Locate and identify every blood parasite.
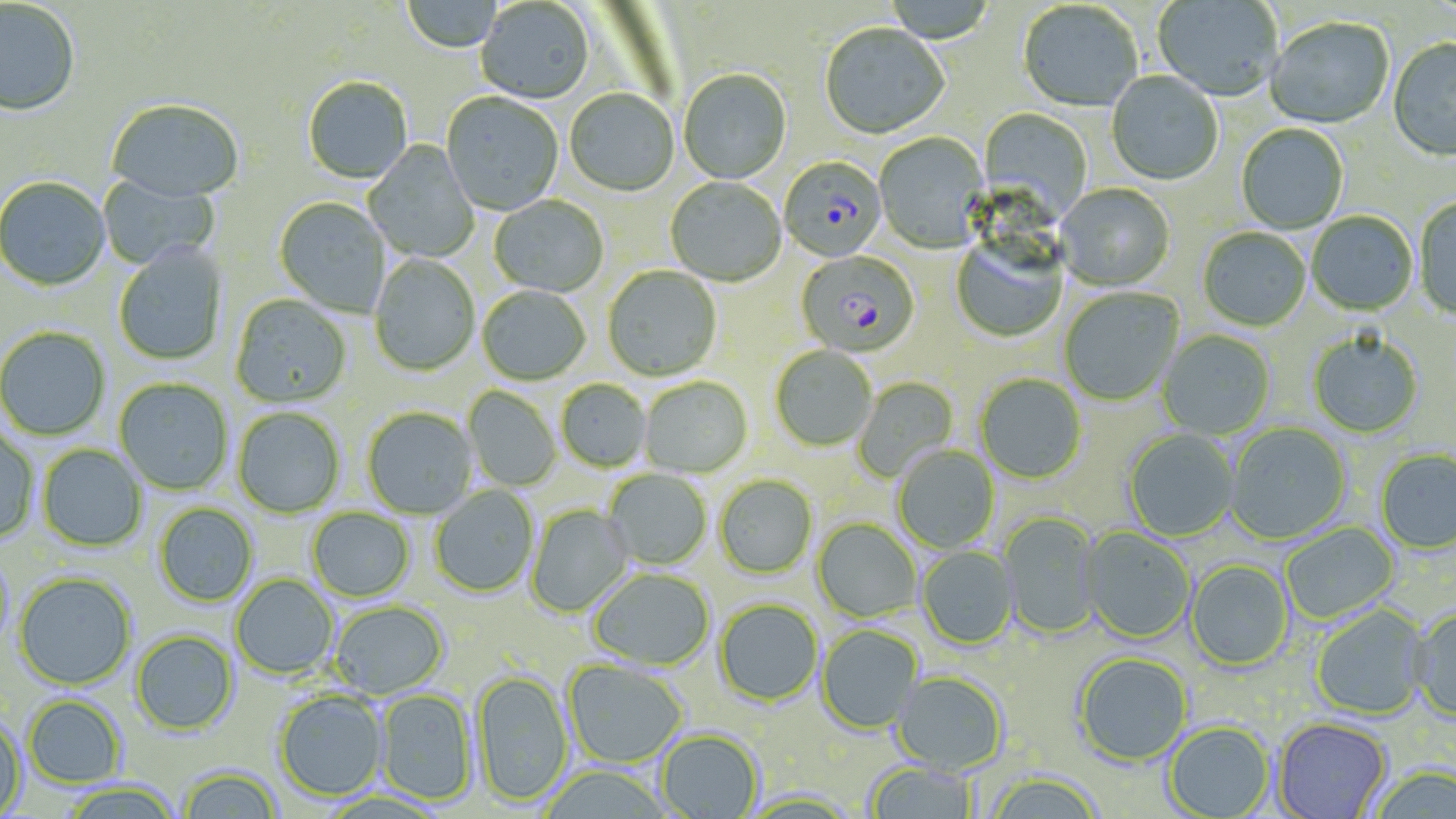
Approximate bounding boxes as (x1, y1, x2, y2) in pixels.
Plasmodium falciparum-infected red blood cells: (779, 158, 886, 263), (796, 251, 919, 358).
No Plasmodium ovale, Plasmodium malariae, Plasmodium vivax, Babesia divergens, or Trypanosoma brucei observed.

Uninfected red blood cell locations: (400, 0, 504, 54), (1153, 0, 1282, 103), (0, 1, 81, 118), (476, 1, 594, 106), (880, 1, 998, 45), (1018, 2, 1142, 113), (1265, 18, 1394, 131), (820, 25, 950, 141), (1388, 39, 1456, 163), (678, 71, 791, 186), (1106, 72, 1223, 187), (303, 78, 413, 186), (565, 91, 679, 198), (441, 94, 563, 217), (106, 101, 245, 206), (978, 108, 1092, 226), (1236, 124, 1349, 235), (874, 133, 989, 254), (363, 141, 480, 263), (97, 173, 219, 271), (0, 178, 110, 292), (665, 178, 786, 288), (1054, 184, 1175, 293), (489, 196, 609, 298), (272, 197, 391, 318), (1414, 197, 1456, 321), (1306, 212, 1418, 317), (1198, 228, 1311, 333), (951, 239, 1069, 343), (113, 245, 228, 365), (370, 255, 480, 377), (603, 267, 721, 382), (477, 287, 591, 386), (1059, 288, 1183, 406), (230, 295, 352, 409), (0, 327, 110, 441), (1158, 331, 1275, 439), (1308, 334, 1422, 439), (770, 347, 877, 453), (975, 374, 1086, 485), (854, 376, 958, 484), (114, 378, 233, 495), (640, 378, 752, 478), (556, 380, 651, 472), (463, 386, 561, 492), (232, 407, 345, 518), (362, 407, 477, 520), (1225, 423, 1350, 545), (0, 428, 40, 545), (1123, 429, 1239, 541), (37, 444, 147, 552), (892, 446, 1000, 553), (1376, 450, 1456, 555), (603, 469, 711, 571), (714, 476, 818, 580), (430, 485, 539, 598), (154, 502, 259, 607), (526, 504, 633, 617), (306, 508, 414, 601), (999, 512, 1101, 639), (812, 519, 920, 623), (1281, 522, 1400, 624), (1079, 528, 1195, 645), (916, 546, 1017, 650), (0, 550, 15, 654), (1186, 560, 1293, 672), (589, 569, 715, 672), (14, 572, 136, 690), (231, 574, 339, 679), (714, 600, 823, 707), (329, 601, 449, 700), (1312, 606, 1430, 721), (1409, 608, 1456, 723), (816, 625, 922, 734), (131, 630, 238, 735), (1074, 654, 1192, 767), (561, 661, 687, 768), (471, 672, 573, 808), (890, 672, 1009, 776), (274, 689, 388, 802), (376, 689, 478, 807), (22, 694, 126, 788), (0, 716, 26, 819), (1273, 718, 1393, 818), (1163, 722, 1274, 819), (655, 730, 763, 819), (865, 762, 978, 819), (177, 765, 283, 818), (539, 766, 670, 819), (1369, 768, 1455, 819), (984, 774, 1105, 819), (59, 780, 183, 818), (741, 792, 862, 818). Slide-level diagnosis: Plasmodium falciparum. Captured at 1000x magnification. One field of a larger specimen. May-Grünwald-Giemsa stain. Thin blood smear. Optical microscopy. Image is 1456×819 pixels.